Report the malaria status of this cell.
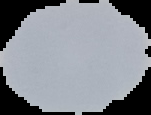

It is uninfected.

Summary:
  - Preparation: thin blood smear
  - Image size: 151×115 pixels
  - Image type: segmented cell region with the area outside set to black